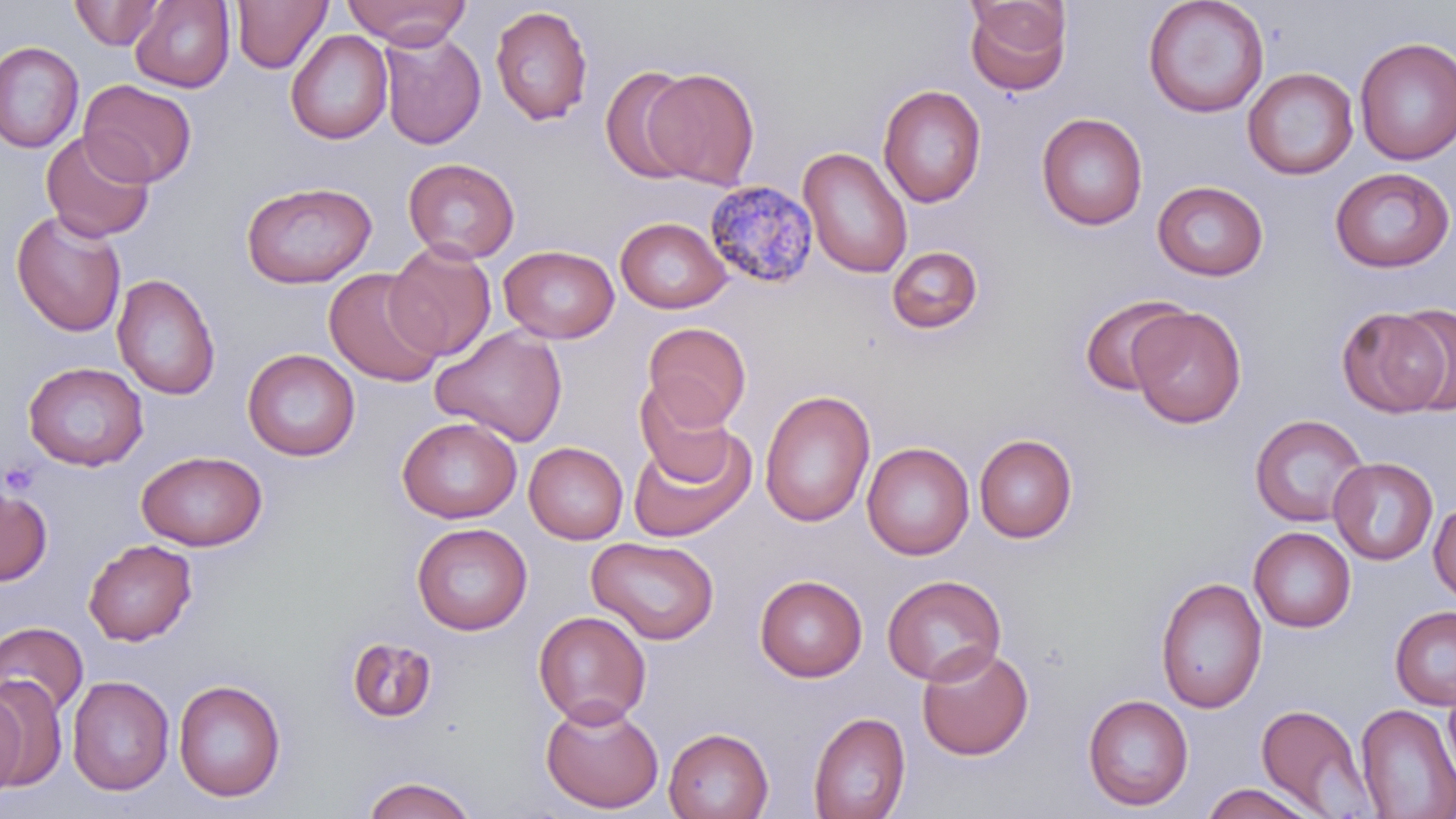
slide-level diagnosis = Plasmodium malariae
field of view = one of a larger specimen
image size = 1456×819 pixels
uninfected red blood cell locations = approximate bounding boxes as named x1/y1/x2/y2 corners in pixels: (x1=232, y1=0, x2=332, y2=73), (x1=341, y1=0, x2=472, y2=49), (x1=1142, y1=0, x2=1269, y2=118), (x1=69, y1=1, x2=165, y2=49), (x1=129, y1=1, x2=235, y2=93), (x1=964, y1=1, x2=1072, y2=96), (x1=490, y1=5, x2=593, y2=126), (x1=286, y1=29, x2=393, y2=145), (x1=378, y1=29, x2=486, y2=150), (x1=1354, y1=36, x2=1456, y2=165), (x1=0, y1=42, x2=84, y2=153), (x1=600, y1=66, x2=701, y2=184), (x1=643, y1=67, x2=760, y2=189), (x1=1242, y1=67, x2=1359, y2=180), (x1=79, y1=80, x2=198, y2=187), (x1=878, y1=84, x2=987, y2=208), (x1=1036, y1=112, x2=1147, y2=230), (x1=40, y1=131, x2=155, y2=242), (x1=798, y1=146, x2=912, y2=278), (x1=403, y1=157, x2=519, y2=263), (x1=1329, y1=167, x2=1455, y2=273), (x1=241, y1=181, x2=377, y2=288), (x1=1152, y1=181, x2=1268, y2=281), (x1=10, y1=210, x2=127, y2=338), (x1=615, y1=216, x2=731, y2=314), (x1=385, y1=241, x2=496, y2=361), (x1=499, y1=245, x2=620, y2=343), (x1=886, y1=246, x2=984, y2=334), (x1=323, y1=268, x2=447, y2=387), (x1=112, y1=273, x2=220, y2=400), (x1=1079, y1=294, x2=1194, y2=397), (x1=1336, y1=306, x2=1450, y2=418), (x1=1129, y1=307, x2=1246, y2=429), (x1=642, y1=321, x2=752, y2=430), (x1=431, y1=326, x2=568, y2=447), (x1=242, y1=348, x2=360, y2=462), (x1=23, y1=361, x2=148, y2=471), (x1=634, y1=379, x2=737, y2=484), (x1=759, y1=388, x2=875, y2=527), (x1=1249, y1=414, x2=1369, y2=527), (x1=396, y1=416, x2=522, y2=523), (x1=629, y1=431, x2=755, y2=542), (x1=974, y1=433, x2=1077, y2=543), (x1=524, y1=442, x2=628, y2=544), (x1=862, y1=442, x2=975, y2=560), (x1=136, y1=450, x2=267, y2=551), (x1=1328, y1=457, x2=1438, y2=565), (x1=0, y1=481, x2=53, y2=586), (x1=1428, y1=501, x2=1456, y2=604), (x1=411, y1=522, x2=532, y2=635), (x1=1249, y1=527, x2=1356, y2=632), (x1=586, y1=537, x2=720, y2=644), (x1=83, y1=539, x2=197, y2=645), (x1=754, y1=574, x2=868, y2=682), (x1=882, y1=574, x2=1006, y2=686), (x1=1155, y1=576, x2=1267, y2=713), (x1=1390, y1=605, x2=1456, y2=710), (x1=532, y1=610, x2=652, y2=727), (x1=0, y1=622, x2=89, y2=717), (x1=345, y1=636, x2=438, y2=723), (x1=917, y1=644, x2=1034, y2=760), (x1=67, y1=675, x2=175, y2=795), (x1=0, y1=676, x2=66, y2=791), (x1=173, y1=678, x2=287, y2=803), (x1=1443, y1=679, x2=1456, y2=784), (x1=0, y1=687, x2=26, y2=799), (x1=1082, y1=693, x2=1193, y2=811), (x1=540, y1=700, x2=664, y2=813), (x1=1255, y1=702, x2=1375, y2=817), (x1=1356, y1=703, x2=1456, y2=818), (x1=809, y1=711, x2=911, y2=819), (x1=663, y1=727, x2=774, y2=819), (x1=361, y1=775, x2=477, y2=819), (x1=1201, y1=782, x2=1322, y2=819)
magnification = 1000x
stain = May-Grünwald-Giemsa
platelet locations = approximate bounding boxes as named x1/y1/x2/y2 corners in pixels: (x1=1, y1=458, x2=42, y2=497)
Plasmodium malariae-infected red blood cell locations = approximate bounding boxes as named x1/y1/x2/y2 corners in pixels: (x1=703, y1=179, x2=818, y2=290)
modality = optical microscopy
preparation = thin blood film